Name the cell type shown.
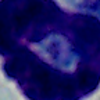
This is a leukocyte.

Captured at 1000x magnification. Micrograph.